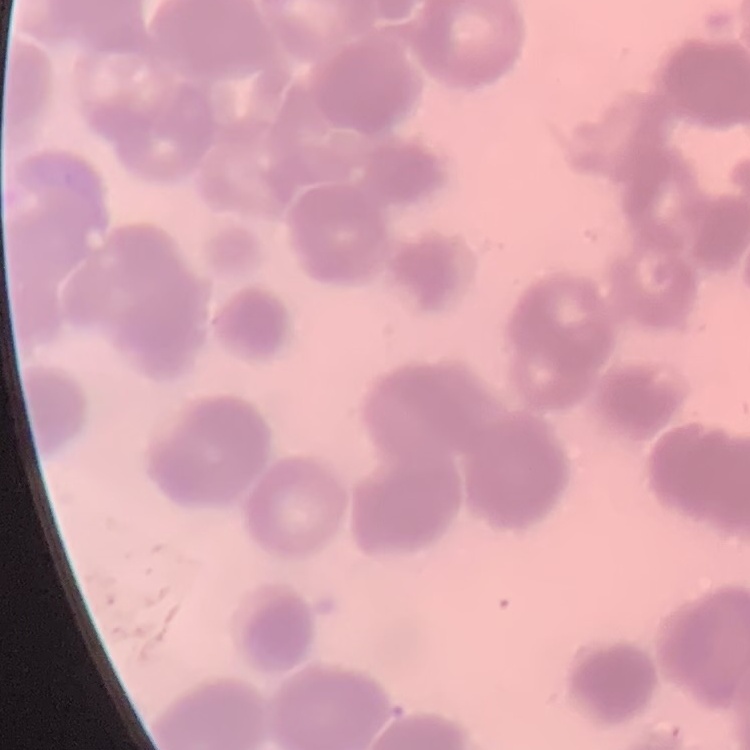
The red blood cells show rouleaux formation. Thin peripheral smear. One tile cut from a larger photomicrograph. Field's or Giemsa stain.